Assess the morphology of the erythrocytes.
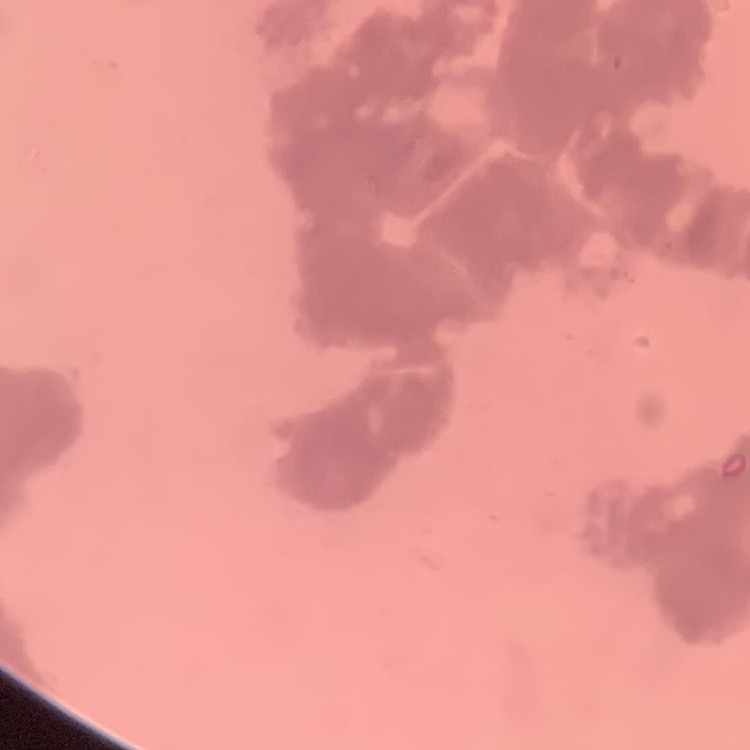
Rouleaux formation.

image_type: square crop of a larger photomicrograph
stain: Field's or Giemsa
preparation: thin blood smear